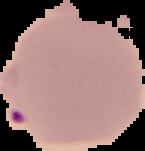
image_type: cell region segmented out of the field of view; surrounding area masked to black
preparation: thin blood film
malaria_status: parasitized
image_size: 145×151 pixels